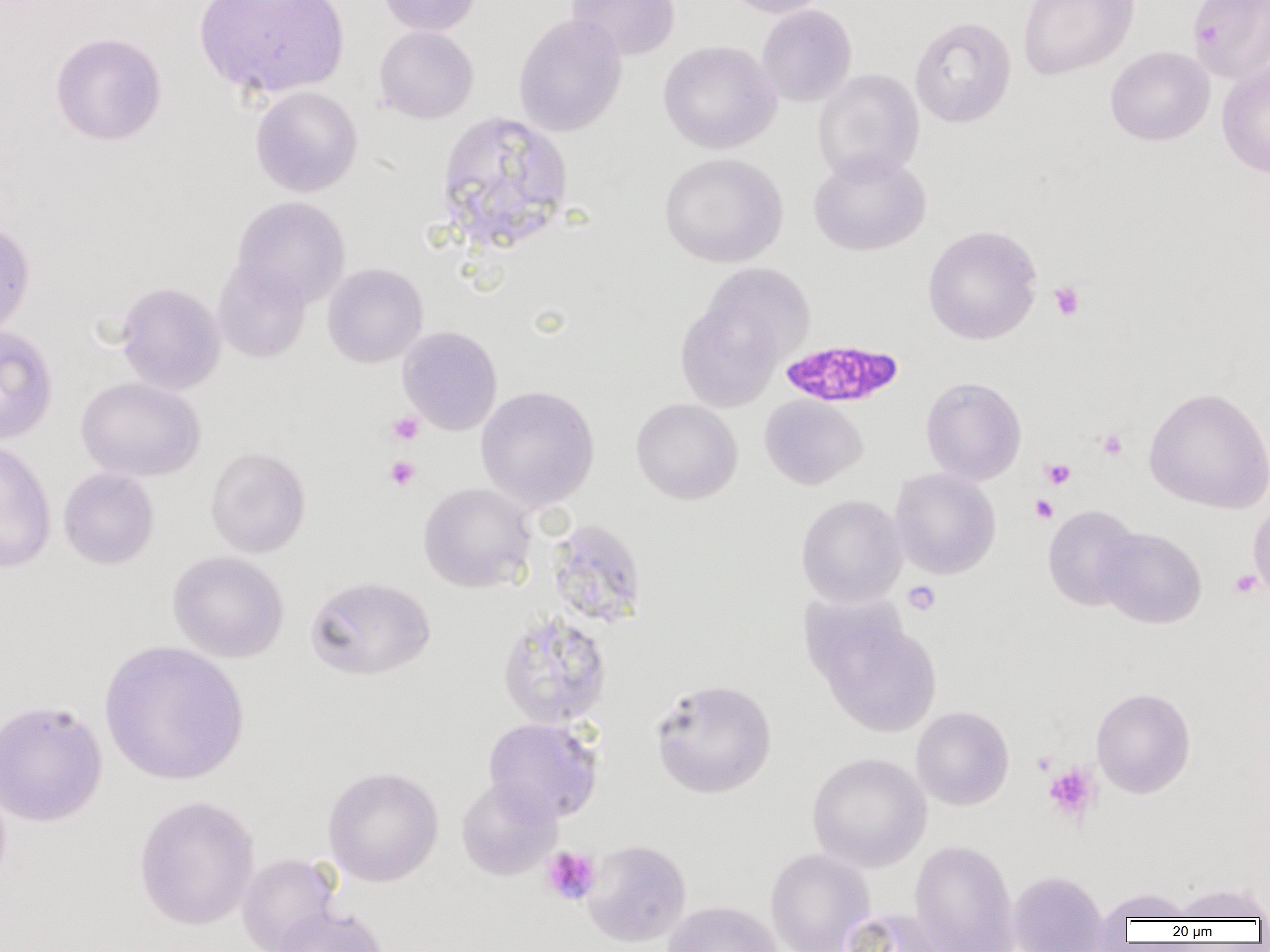
Approximate bounding boxes as named x1/y1/x2/y2 corners in pixels. Platelet locations: (x1=1049, y1=281, x2=1085, y2=321), (x1=386, y1=411, x2=424, y2=446), (x1=1096, y1=428, x2=1128, y2=461), (x1=385, y1=456, x2=420, y2=490), (x1=1040, y1=458, x2=1076, y2=490), (x1=1030, y1=494, x2=1058, y2=523), (x1=1229, y1=569, x2=1263, y2=599), (x1=903, y1=581, x2=941, y2=616), (x1=1032, y1=752, x2=1055, y2=775), (x1=1043, y1=763, x2=1101, y2=823), (x1=541, y1=845, x2=601, y2=905). Plasmodium falciparum-infected red blood cell locations: (x1=779, y1=338, x2=903, y2=409). Uninfected red blood cell locations: (x1=194, y1=0, x2=350, y2=99), (x1=377, y1=0, x2=483, y2=36), (x1=566, y1=0, x2=680, y2=61), (x1=718, y1=0, x2=834, y2=18), (x1=1017, y1=0, x2=1139, y2=81), (x1=1187, y1=0, x2=1270, y2=83), (x1=756, y1=4, x2=857, y2=108), (x1=513, y1=14, x2=627, y2=137), (x1=909, y1=16, x2=1017, y2=129), (x1=373, y1=26, x2=478, y2=124), (x1=50, y1=31, x2=166, y2=146), (x1=658, y1=39, x2=781, y2=154), (x1=1105, y1=46, x2=1215, y2=146), (x1=1217, y1=59, x2=1270, y2=179), (x1=812, y1=68, x2=924, y2=184), (x1=249, y1=86, x2=362, y2=197), (x1=435, y1=110, x2=574, y2=254), (x1=808, y1=150, x2=931, y2=256), (x1=659, y1=152, x2=788, y2=268), (x1=232, y1=196, x2=351, y2=308), (x1=0, y1=218, x2=36, y2=338), (x1=922, y1=225, x2=1042, y2=344), (x1=212, y1=259, x2=311, y2=362), (x1=701, y1=261, x2=816, y2=365), (x1=322, y1=263, x2=427, y2=367), (x1=115, y1=281, x2=226, y2=395), (x1=675, y1=294, x2=786, y2=412), (x1=0, y1=325, x2=58, y2=445), (x1=398, y1=326, x2=502, y2=435), (x1=920, y1=376, x2=1026, y2=485), (x1=76, y1=377, x2=206, y2=481), (x1=475, y1=385, x2=600, y2=510), (x1=1144, y1=386, x2=1270, y2=514), (x1=759, y1=394, x2=868, y2=490), (x1=631, y1=398, x2=743, y2=504), (x1=0, y1=440, x2=56, y2=573), (x1=205, y1=446, x2=311, y2=557), (x1=58, y1=467, x2=159, y2=569), (x1=889, y1=467, x2=1001, y2=580), (x1=418, y1=482, x2=537, y2=593), (x1=796, y1=494, x2=907, y2=607), (x1=1248, y1=501, x2=1270, y2=598), (x1=1042, y1=504, x2=1143, y2=611), (x1=547, y1=519, x2=648, y2=629), (x1=1096, y1=527, x2=1207, y2=629), (x1=168, y1=551, x2=288, y2=662), (x1=305, y1=575, x2=436, y2=681), (x1=497, y1=610, x2=613, y2=729), (x1=813, y1=610, x2=941, y2=736), (x1=99, y1=640, x2=249, y2=786), (x1=649, y1=678, x2=777, y2=799), (x1=1091, y1=687, x2=1196, y2=798), (x1=0, y1=698, x2=107, y2=827), (x1=911, y1=706, x2=1014, y2=810), (x1=483, y1=717, x2=603, y2=824), (x1=806, y1=752, x2=931, y2=872), (x1=322, y1=766, x2=444, y2=887), (x1=455, y1=777, x2=561, y2=881), (x1=133, y1=794, x2=260, y2=931), (x1=582, y1=838, x2=691, y2=947), (x1=910, y1=840, x2=1019, y2=952), (x1=765, y1=848, x2=874, y2=952), (x1=237, y1=853, x2=341, y2=952), (x1=1007, y1=871, x2=1109, y2=952), (x1=1170, y1=881, x2=1269, y2=922), (x1=1094, y1=886, x2=1199, y2=928), (x1=663, y1=900, x2=783, y2=952), (x1=273, y1=904, x2=390, y2=952), (x1=838, y1=907, x2=956, y2=952). Slide-level diagnosis: Plasmodium falciparum. Image is 1270×952 pixels. Thin blood film. Captured at 1000x magnification. Light microscopy. One field of a larger specimen.